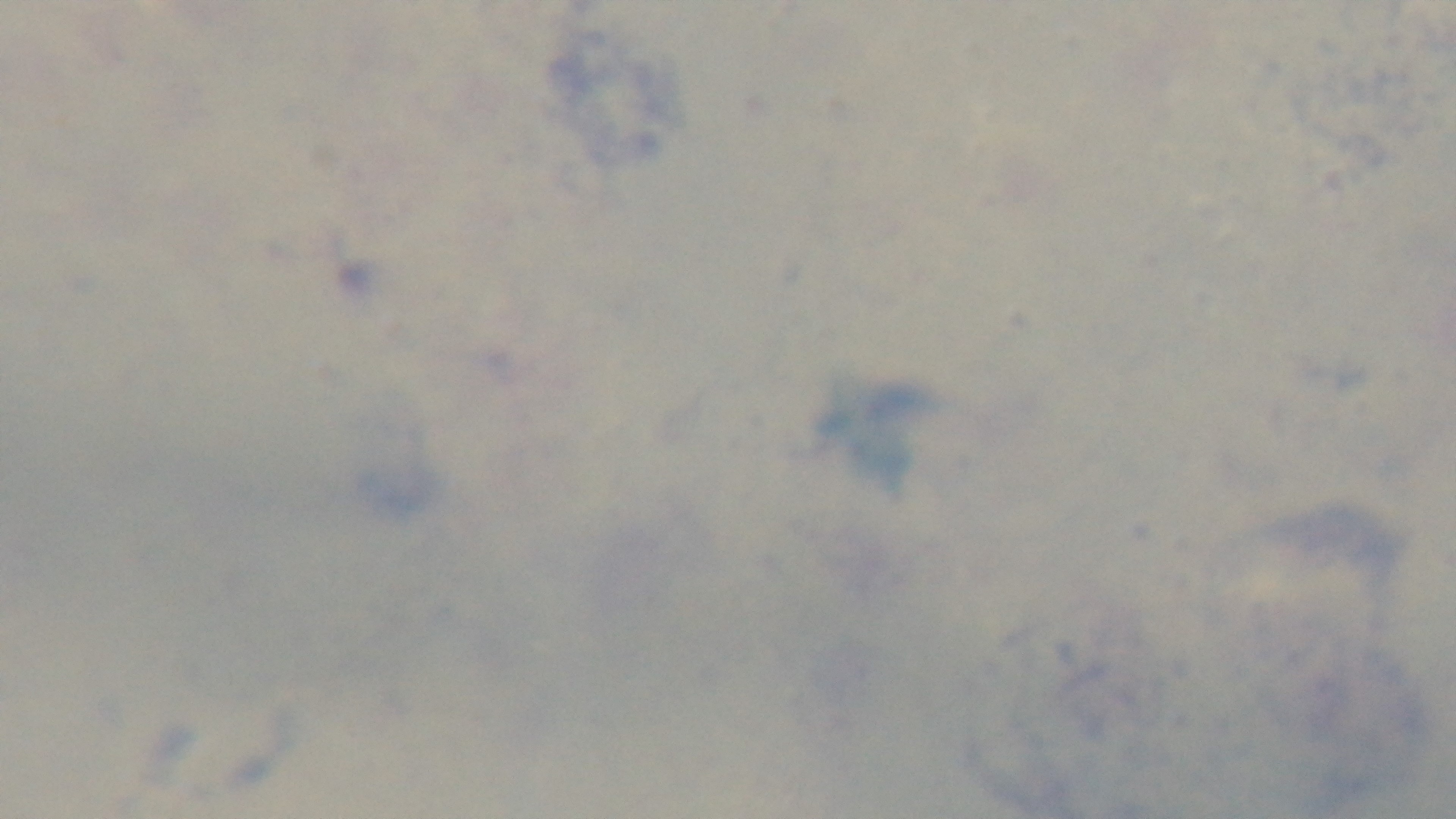
{
  "malaria_status": "negative",
  "preparation": "thick blood film",
  "stain": "Giemsa",
  "objective": "100x oil immersion",
  "capture": "mounted 4K digital camera",
  "field_of_view": "one from the slide",
  "modality": "light microscopy"
}